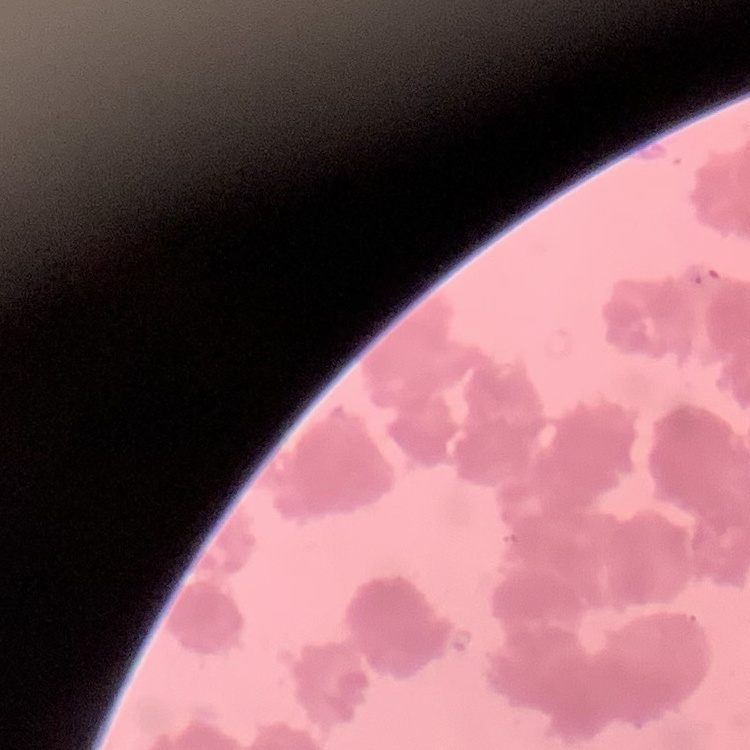

red blood cell morphology = rouleaux formation
preparation = thin blood smear
stain = Field's or Giemsa
image type = square crop of a larger photomicrograph